Point out each Plasmodium parasite.
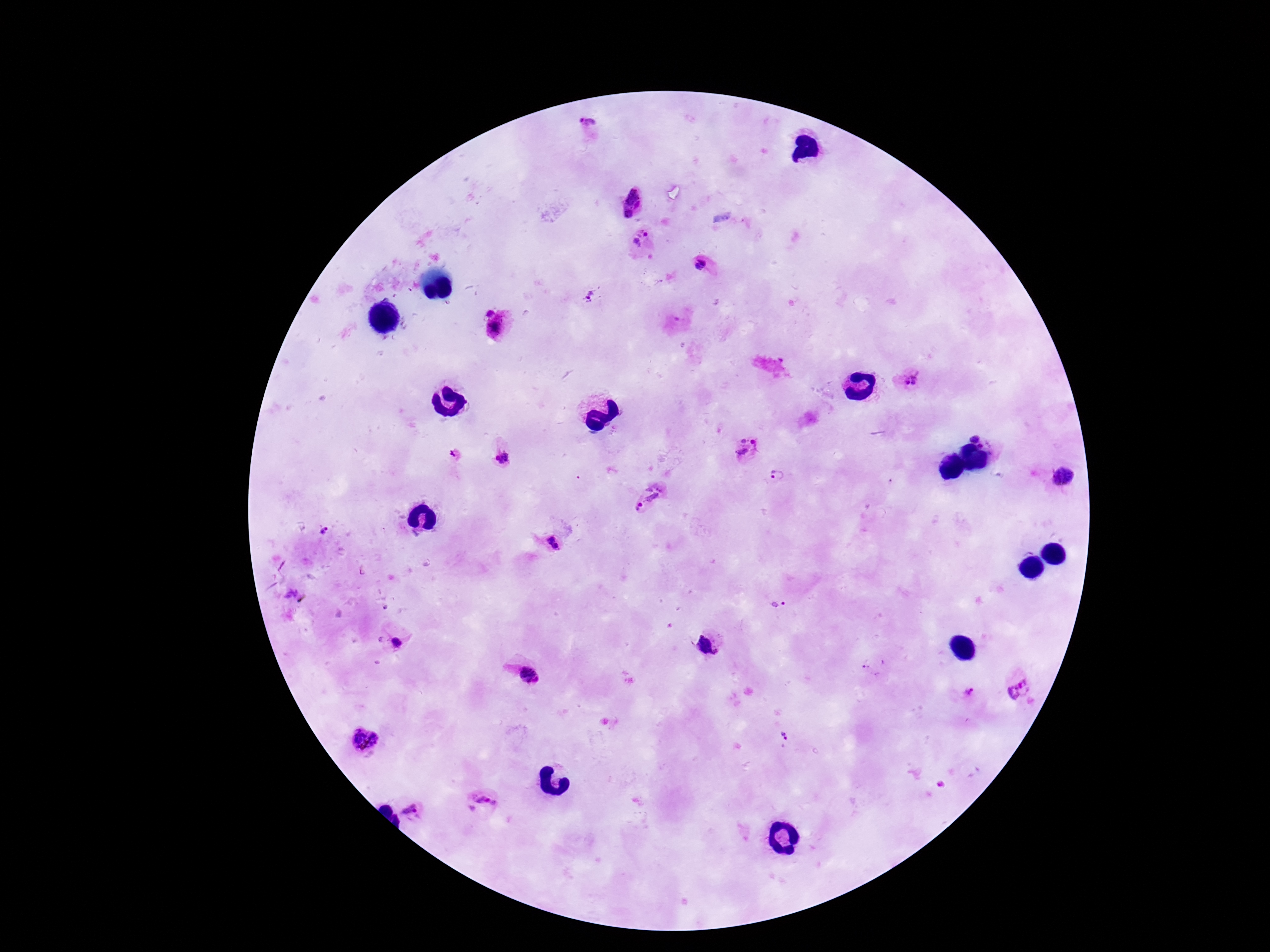
Approximate centers as {x, y} in pixels.
Plasmodium parasites: {587, 124}, {634, 197}, {627, 215}, {642, 240}, {700, 266}, {588, 296}, {494, 331}, {914, 378}, {977, 435}, {983, 446}, {747, 448}, {991, 454}, {454, 455}, {501, 458}, {778, 475}, {1062, 476}, {646, 498}, {325, 532}, {550, 539}, {556, 546}, {778, 607}, {396, 644}, {707, 645}, {874, 667}, {529, 676}, {1018, 688}, {968, 692}, {784, 735}, {364, 740}, {483, 804}, {413, 812}.

Summary:
  - Stain: Giemsa
  - Patient malaria status: positive
  - Image size: 1270×952 pixels
  - Capture: smartphone camera through the microscope eyepiece
  - Preparation: thick blood film
  - Magnification: 100x
  - Field of view: one from this slide